Outline each blood parasite and name the species.
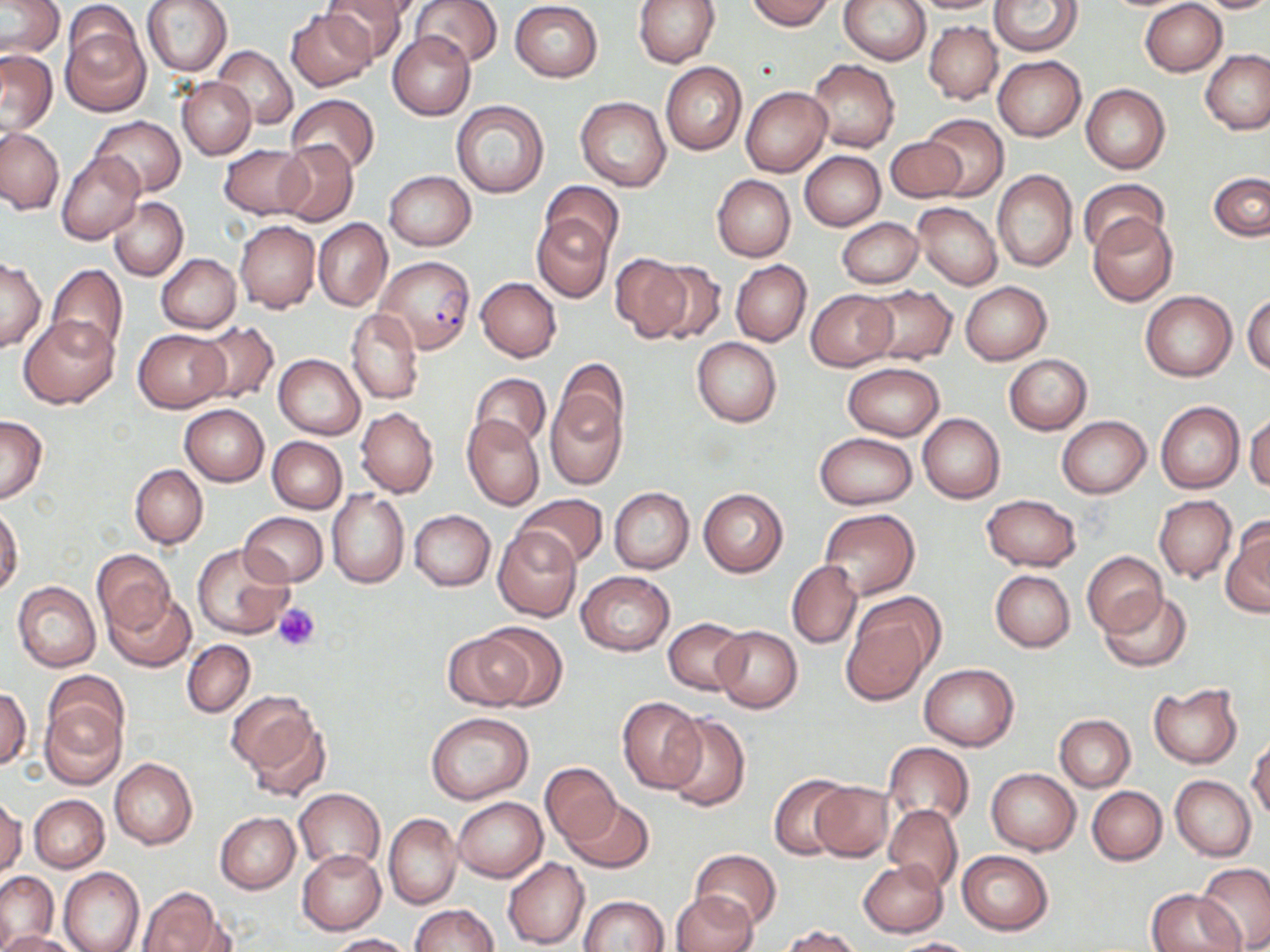
Approximate bounding boxes as (x1, y1, x2, y2) in pixels.
Plasmodium falciparum-infected red blood cells: (376, 255, 477, 354).
No Plasmodium ovale, Plasmodium malariae, Plasmodium vivax, Babesia divergens, or Trypanosoma brucei observed.

Uninfected red blood cell locations: (141, 0, 232, 76), (322, 0, 412, 63), (331, 0, 417, 24), (410, 0, 503, 67), (634, 0, 719, 67), (746, 0, 834, 29), (839, 0, 930, 64), (908, 0, 1006, 14), (990, 0, 1082, 56), (1194, 0, 1270, 13), (1, 1, 64, 57), (1140, 1, 1227, 76), (510, 2, 604, 82), (286, 8, 377, 91), (61, 17, 149, 115), (923, 21, 1002, 104), (388, 32, 476, 120), (212, 45, 297, 130), (1201, 49, 1269, 135), (0, 51, 57, 133), (992, 55, 1086, 142), (807, 59, 900, 153), (660, 62, 747, 155), (178, 77, 256, 159), (1082, 83, 1170, 173), (741, 85, 832, 177), (286, 94, 380, 177), (576, 96, 671, 192), (450, 99, 551, 198), (919, 115, 1009, 200), (91, 117, 185, 196), (0, 127, 64, 214), (885, 136, 966, 203), (275, 140, 358, 227), (219, 145, 310, 218), (56, 151, 144, 244), (801, 151, 885, 229), (993, 170, 1078, 272), (385, 171, 476, 250), (1209, 173, 1269, 241), (712, 175, 795, 261), (1078, 179, 1169, 257), (540, 181, 624, 261), (107, 197, 188, 281), (913, 202, 1002, 289), (1087, 213, 1178, 306), (532, 214, 612, 303), (314, 218, 391, 311), (836, 218, 924, 287), (234, 220, 321, 313), (156, 253, 241, 333), (610, 253, 695, 341), (1, 257, 45, 352), (731, 260, 811, 346), (650, 262, 724, 345), (46, 264, 128, 357), (476, 277, 561, 362), (960, 281, 1051, 363), (861, 285, 957, 365), (807, 289, 896, 371), (1140, 291, 1237, 381), (1244, 292, 1270, 378), (345, 308, 424, 405), (19, 315, 119, 408), (194, 320, 279, 406), (133, 328, 230, 412), (691, 337, 781, 428), (274, 354, 365, 439), (1005, 354, 1092, 434), (554, 359, 628, 445), (842, 363, 944, 441), (826, 366, 938, 507), (470, 373, 551, 451), (546, 390, 625, 490), (1155, 401, 1245, 494), (179, 404, 268, 487), (356, 407, 438, 498), (918, 413, 1005, 504), (1245, 413, 1270, 493), (0, 415, 47, 503), (462, 415, 545, 511), (1056, 416, 1151, 497), (813, 432, 915, 509), (268, 436, 347, 512), (130, 464, 208, 548), (608, 487, 694, 573), (698, 488, 788, 577), (328, 489, 409, 588), (513, 493, 609, 569), (981, 494, 1081, 571), (1155, 496, 1236, 583), (0, 506, 23, 598), (819, 508, 919, 598), (409, 509, 496, 591), (239, 512, 327, 586), (1221, 520, 1270, 617), (494, 526, 582, 620), (193, 543, 294, 639), (92, 550, 175, 634), (1082, 551, 1167, 636), (786, 560, 862, 650), (989, 569, 1075, 651), (577, 570, 675, 656), (13, 582, 101, 671), (106, 590, 195, 672), (1098, 590, 1191, 671), (841, 604, 937, 703), (664, 618, 750, 694), (477, 623, 568, 709), (713, 626, 802, 712), (444, 630, 534, 710), (183, 640, 255, 717), (919, 663, 1020, 750), (43, 670, 128, 749), (1149, 684, 1242, 769), (0, 687, 31, 770), (39, 696, 126, 788), (617, 696, 705, 793), (233, 699, 329, 800), (426, 712, 534, 803), (663, 715, 751, 812), (1054, 715, 1134, 791), (1248, 738, 1270, 820), (882, 742, 973, 829), (109, 757, 198, 849), (541, 763, 619, 845), (986, 768, 1080, 854), (770, 774, 855, 860), (1170, 776, 1256, 860), (811, 781, 894, 861), (1087, 785, 1167, 864), (293, 788, 384, 872), (28, 794, 109, 872), (0, 796, 25, 875), (453, 797, 546, 882), (566, 798, 654, 873), (884, 804, 963, 891), (215, 812, 300, 893), (384, 813, 462, 910), (298, 849, 387, 934), (689, 850, 782, 929), (956, 850, 1053, 935), (502, 857, 589, 949), (859, 858, 947, 936), (1196, 864, 1270, 951), (59, 867, 144, 952), (0, 870, 57, 950), (137, 887, 228, 952), (1147, 888, 1240, 952), (672, 892, 756, 952), (580, 895, 669, 951), (410, 904, 497, 952), (778, 925, 865, 952), (1, 931, 77, 952), (326, 933, 416, 952), (892, 937, 977, 951). Platelet locations: (273, 604, 320, 651). Slide-level diagnosis: Plasmodium falciparum. One field of a larger specimen. 1000x magnification. May-Grünwald-Giemsa-stained preparation. Thin blood film. Image is 1270×952 pixels. Light microscopy.